Identify the parasite.
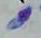
This is Toxoplasma gondii.

modality = photomicrograph
magnification = 1000x